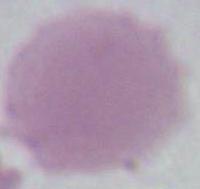

identification: red blood cell
modality: micrograph
magnification: 1000x